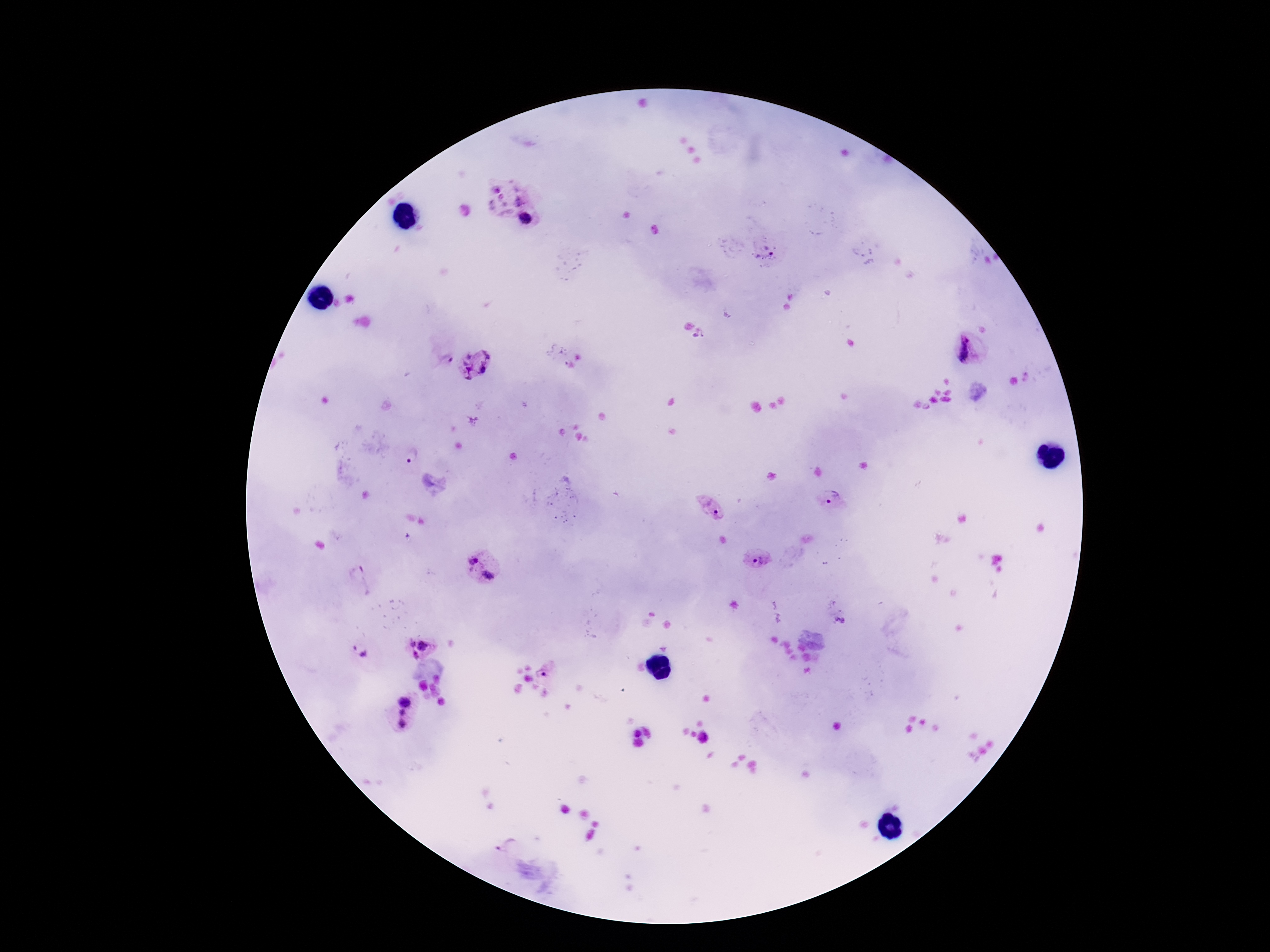

Plasmodium parasite locations = approximate centers as [x, y] in pixels: [506, 194], [527, 219], [766, 252], [699, 336], [969, 352], [557, 356], [446, 358], [476, 362], [411, 456], [833, 501], [711, 507], [756, 560], [473, 561], [488, 575], [359, 579], [838, 616], [412, 644], [422, 645], [354, 648], [364, 654], [415, 655], [546, 674], [404, 701], [402, 712], [403, 723], [502, 841]
stain = Giemsa
capture = smartphone camera through the microscope eyepiece
patient malaria status = infected
preparation = thick blood film
field of view = one from this slide
magnification = 100x
image size = 1270×952 pixels